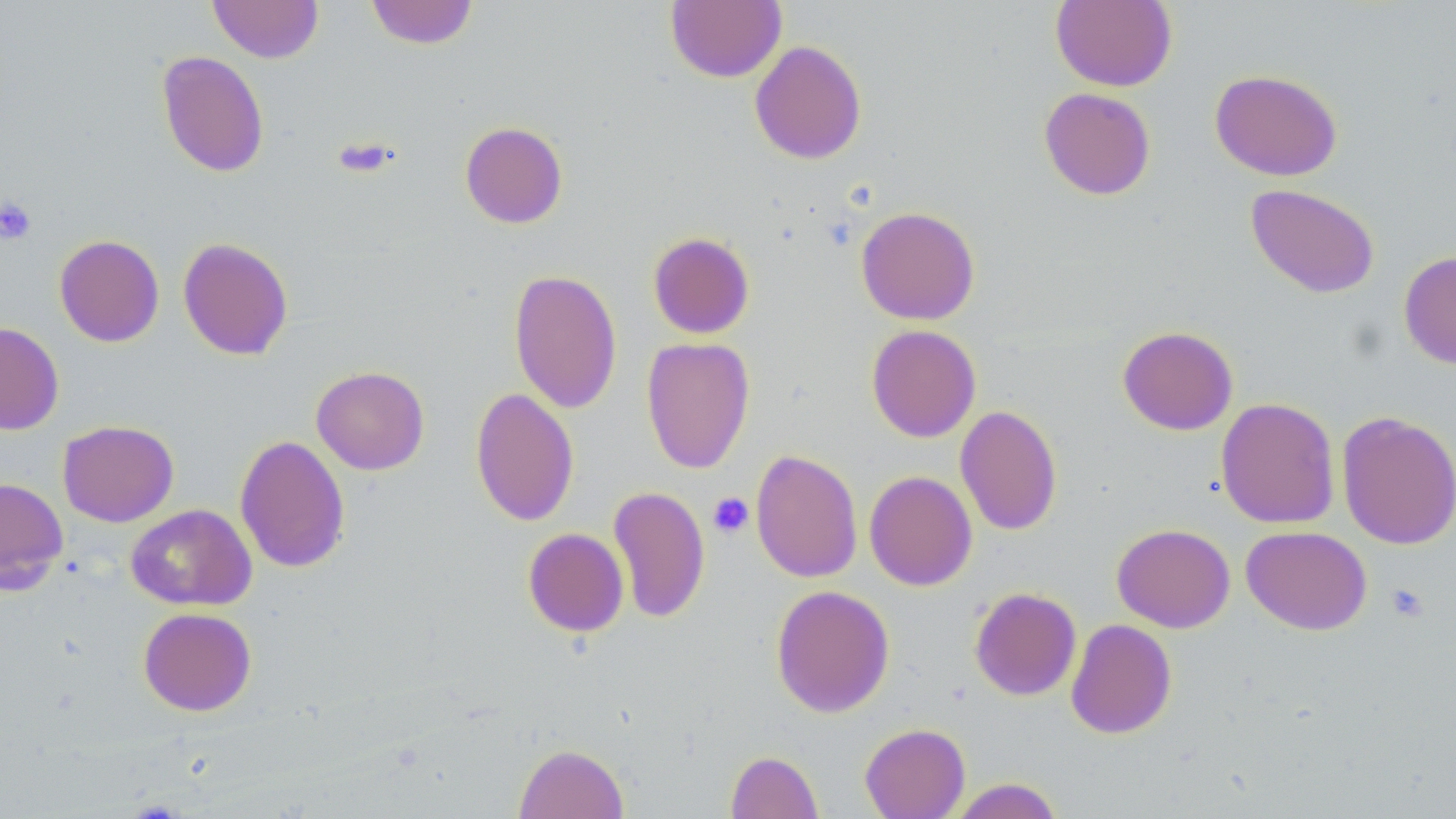 Approximate bounding boxes as named x1/y1/x2/y2 corners in pixels. Platelet locations: (x1=0, y1=198, x2=36, y2=245), (x1=709, y1=493, x2=754, y2=538), (x1=1386, y1=583, x2=1430, y2=623). Uninfected red blood cell locations: (x1=209, y1=0, x2=323, y2=63), (x1=365, y1=0, x2=479, y2=49), (x1=1050, y1=0, x2=1177, y2=91), (x1=665, y1=1, x2=786, y2=83), (x1=749, y1=40, x2=867, y2=164), (x1=156, y1=50, x2=269, y2=178), (x1=1209, y1=68, x2=1342, y2=181), (x1=1039, y1=87, x2=1156, y2=200), (x1=459, y1=121, x2=568, y2=229), (x1=1245, y1=183, x2=1380, y2=299), (x1=856, y1=206, x2=980, y2=325), (x1=647, y1=231, x2=755, y2=339), (x1=54, y1=235, x2=164, y2=347), (x1=177, y1=238, x2=293, y2=361), (x1=1398, y1=250, x2=1456, y2=369), (x1=508, y1=269, x2=622, y2=414), (x1=0, y1=321, x2=64, y2=434), (x1=866, y1=324, x2=981, y2=443), (x1=1117, y1=326, x2=1238, y2=435), (x1=641, y1=337, x2=755, y2=474), (x1=311, y1=366, x2=429, y2=475), (x1=470, y1=387, x2=580, y2=527), (x1=1216, y1=397, x2=1340, y2=529), (x1=955, y1=404, x2=1062, y2=536), (x1=1336, y1=410, x2=1456, y2=550), (x1=57, y1=420, x2=179, y2=527), (x1=235, y1=434, x2=350, y2=574), (x1=750, y1=449, x2=863, y2=583), (x1=863, y1=470, x2=977, y2=591), (x1=0, y1=477, x2=69, y2=594), (x1=608, y1=486, x2=710, y2=624), (x1=126, y1=504, x2=257, y2=611), (x1=1112, y1=523, x2=1235, y2=633), (x1=1241, y1=526, x2=1372, y2=635), (x1=522, y1=528, x2=629, y2=637), (x1=770, y1=584, x2=895, y2=718), (x1=969, y1=587, x2=1082, y2=701), (x1=138, y1=607, x2=256, y2=716), (x1=1065, y1=619, x2=1177, y2=739), (x1=859, y1=722, x2=970, y2=818), (x1=514, y1=743, x2=628, y2=818), (x1=726, y1=750, x2=823, y2=818), (x1=948, y1=778, x2=1065, y2=818). Slide-level diagnosis: negative for blood parasites. May-Grünwald-Giemsa-stained preparation. Thin blood smear. 1000x magnification. Image is 1456×819 pixels. Optical microscopy. One field of a larger specimen.